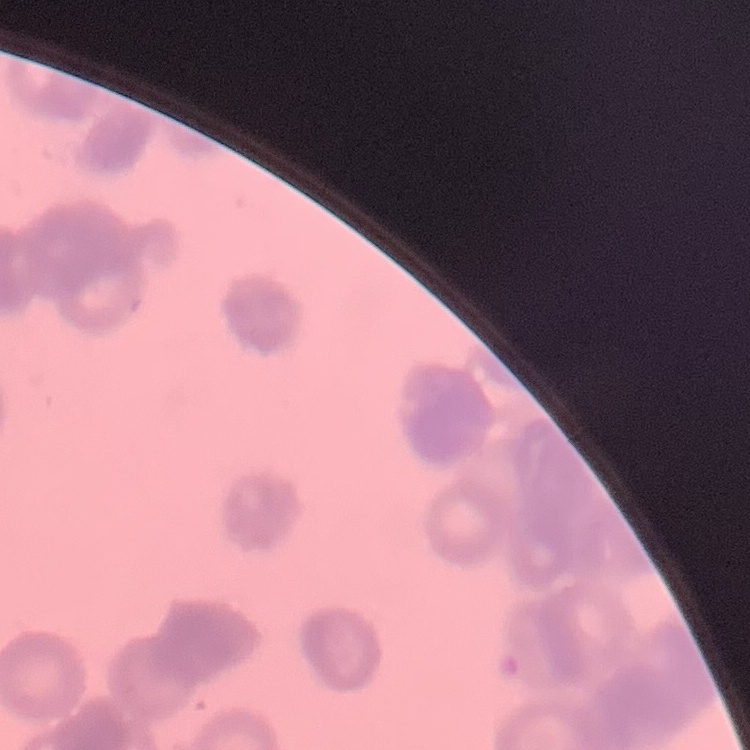

The erythrocytes exhibit rouleaux formation. One tile cut from a larger photomicrograph. Thin blood film. Stained with either Field's or Giemsa.